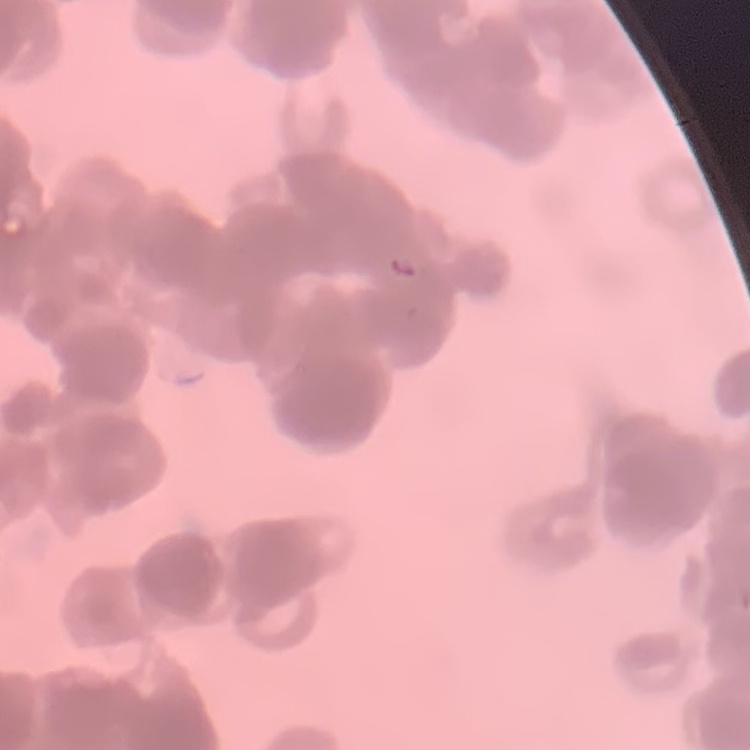

erythrocyte morphology = rouleaux formation
stain = Field's or Giemsa
preparation = thin blood smear
image type = square crop of a larger photomicrograph